State which parasite is depicted.
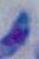

Toxoplasma gondii.

modality = micrograph
magnification = 1000x